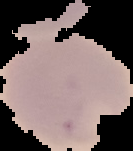 The area outside the segmented cell region is set to black. From a thin blood smear. Image is 133×151 pixels. Malaria status: parasitized.